Report the malaria status of this cell.
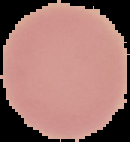
It is uninfected.

Summary:
  - Image type: segmented cell region on a black background
  - Preparation: thin blood film
  - Image size: 130×142 pixels